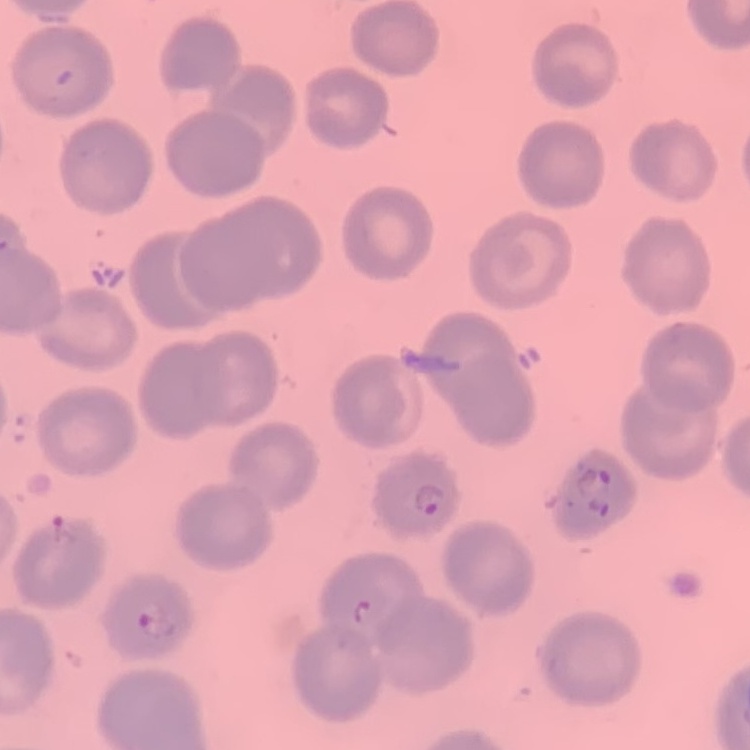
The erythrocytes show no rouleaux formation. Thin peripheral smear. Field's or Giemsa stain. Square crop of a larger photomicrograph.